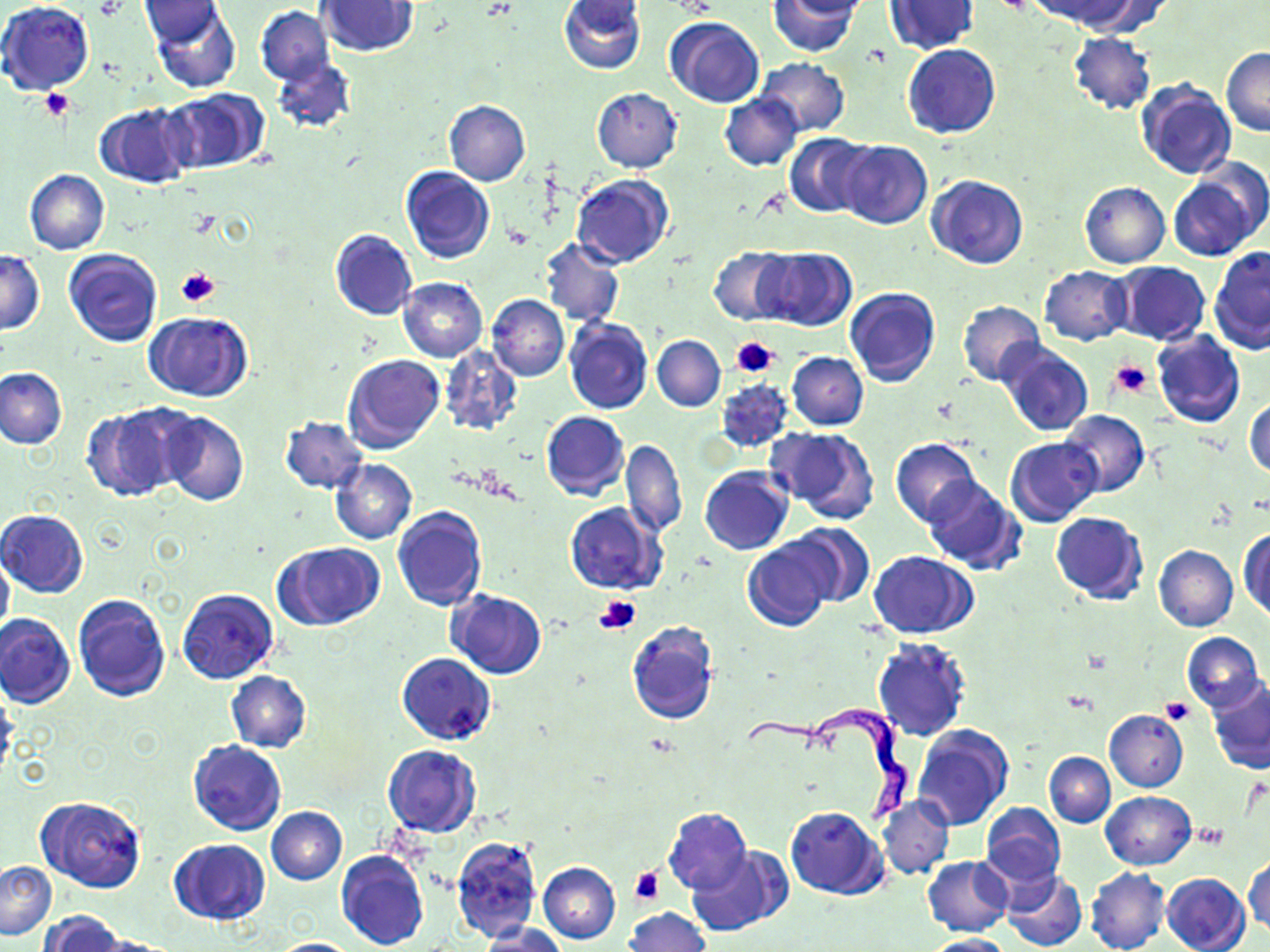
Approximate bounding boxes as (x1, y1, x2, y2) in pixels. Trypanosoma brucei locations: (745, 701, 912, 834). Uninfected red blood cell locations: (559, 0, 645, 74), (767, 0, 860, 57), (775, 0, 874, 19), (1045, 0, 1153, 34), (0, 1, 94, 95), (139, 1, 225, 47), (319, 1, 418, 56), (882, 1, 979, 55), (151, 3, 241, 94), (255, 7, 333, 85), (664, 17, 765, 108), (1068, 33, 1157, 114), (902, 44, 999, 138), (1221, 48, 1270, 135), (272, 58, 356, 134), (756, 59, 849, 137), (1134, 79, 1237, 182), (592, 88, 682, 172), (161, 89, 267, 174), (720, 93, 802, 170), (443, 99, 530, 186), (94, 103, 194, 189), (784, 132, 872, 217), (837, 140, 932, 229), (1194, 156, 1270, 240), (401, 166, 495, 264), (26, 169, 109, 254), (927, 174, 1027, 269), (570, 175, 673, 269), (1169, 177, 1256, 260), (1080, 182, 1170, 268), (329, 229, 417, 321), (540, 238, 625, 326), (1209, 245, 1270, 353), (708, 246, 795, 325), (755, 247, 856, 331), (64, 249, 162, 346), (0, 250, 43, 334), (1110, 261, 1209, 345), (1040, 266, 1130, 346), (398, 277, 488, 362), (845, 288, 940, 387), (486, 294, 568, 381), (957, 300, 1046, 386), (144, 312, 253, 402), (564, 318, 652, 415), (1152, 330, 1245, 428), (653, 335, 725, 412), (998, 342, 1093, 437), (439, 344, 523, 437), (787, 352, 867, 430), (343, 354, 444, 454), (1, 368, 67, 448), (717, 380, 794, 452), (1245, 397, 1270, 476), (82, 405, 187, 502), (1059, 410, 1148, 496), (159, 411, 249, 507), (540, 411, 628, 501), (281, 417, 367, 493), (765, 427, 880, 522), (1006, 436, 1102, 526), (621, 439, 688, 538), (891, 439, 981, 527), (330, 459, 418, 544), (700, 465, 794, 554), (923, 474, 1025, 575), (564, 502, 665, 595), (392, 507, 487, 612), (0, 510, 89, 597), (1051, 511, 1148, 605), (784, 523, 875, 607), (1239, 528, 1269, 621), (742, 540, 833, 632), (274, 542, 382, 630), (1154, 544, 1238, 632), (870, 551, 977, 638), (0, 552, 14, 642), (178, 589, 277, 685), (447, 590, 546, 679), (74, 593, 170, 701), (0, 614, 75, 709), (626, 621, 720, 725), (1182, 632, 1266, 711), (871, 636, 972, 742), (396, 652, 495, 745), (227, 671, 310, 752), (1208, 680, 1270, 774), (0, 690, 19, 782), (1105, 710, 1188, 791), (912, 725, 1011, 829), (187, 741, 286, 836), (383, 746, 481, 837), (1044, 752, 1115, 827), (1101, 791, 1195, 870), (878, 795, 955, 880), (36, 796, 145, 892), (979, 801, 1066, 891), (267, 806, 347, 884), (785, 806, 887, 899), (663, 807, 753, 895), (452, 836, 541, 941), (168, 839, 269, 926), (687, 846, 789, 936), (337, 850, 429, 950), (1244, 853, 1269, 938), (922, 856, 1013, 936), (1, 861, 56, 940), (539, 862, 620, 943), (1085, 866, 1170, 952), (1002, 870, 1086, 951), (1161, 872, 1251, 952), (624, 907, 708, 952), (40, 911, 122, 952), (481, 925, 567, 952), (917, 934, 1013, 951), (86, 935, 185, 951), (266, 938, 360, 950). Platelet locations: (41, 89, 75, 121), (177, 268, 218, 307), (731, 334, 779, 379), (1111, 358, 1153, 400), (595, 594, 642, 633), (1161, 697, 1194, 723), (1196, 823, 1228, 849), (630, 868, 663, 905). Slide-level diagnosis: Trypanosoma brucei. Optical microscopy. Thin blood film. One field of a larger specimen. May-Grünwald-Giemsa stain. Image is 1270×952 pixels. Captured at 1000x magnification.